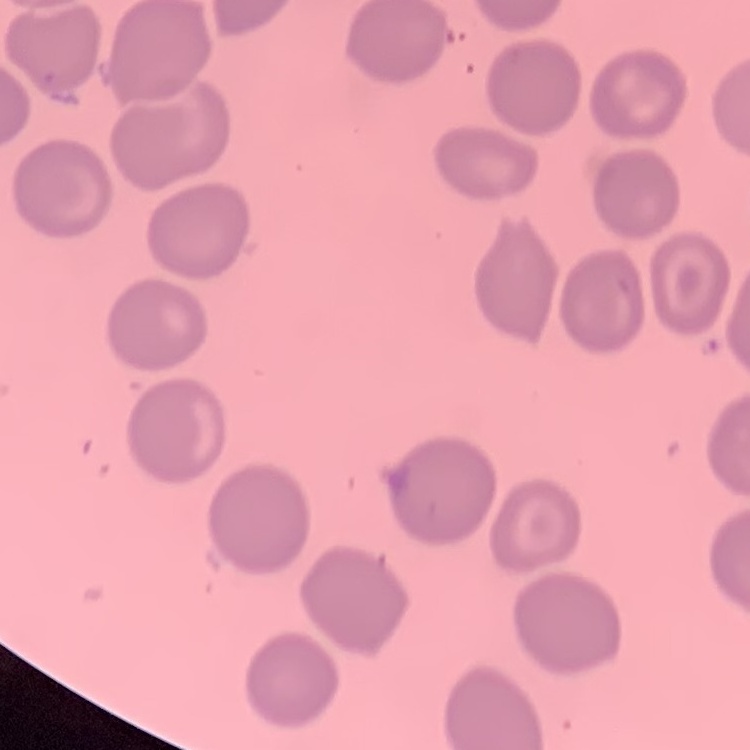
erythrocyte morphology = no rouleaux formation
image type = one tile cut from a larger photomicrograph
preparation = thin peripheral smear
stain = Field's or Giemsa